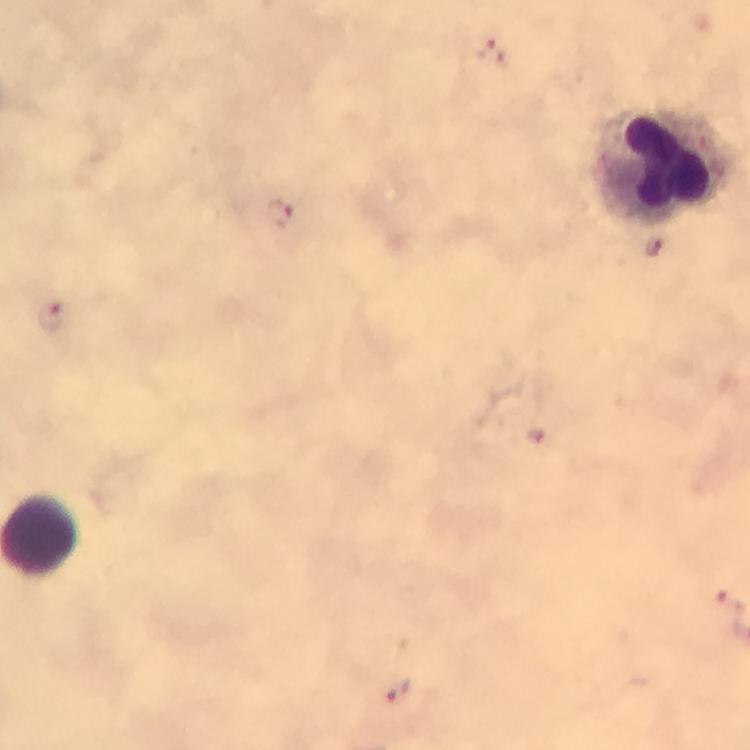
preparation: thick blood smear
image_size: 750×750 pixels
magnification: 100x
cropped_from: a single field of view
malaria_parasite_locations: 'approximate centers as (x, y) in pixels: (491, 50), (278, 214), (654, 247), (51, 316), (727, 599), (402, 692)'
context: from a malaria diagnostic workup
capture: smartphone photograph through a microscope
immersion_oil: applied
leukocyte_locations: 'approximate centers as (x, y) in pixels: (666, 162)'
stain: Giemsa